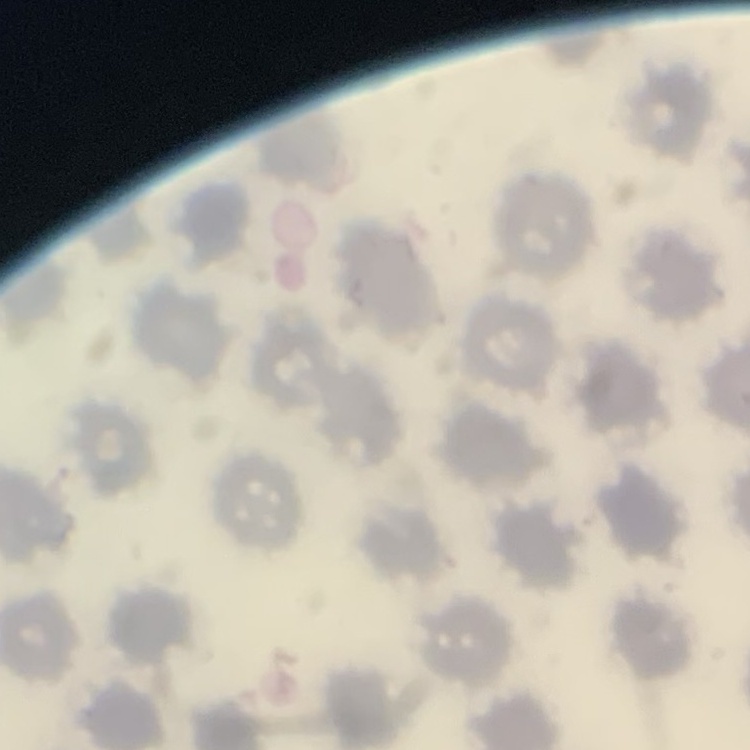

{
  "erythrocyte_morphology": "no rouleaux formation",
  "stain": "Field's or Giemsa",
  "image_type": "one tile cut from a larger photomicrograph",
  "preparation": "thin blood film"
}